Identify the blood parasite species.
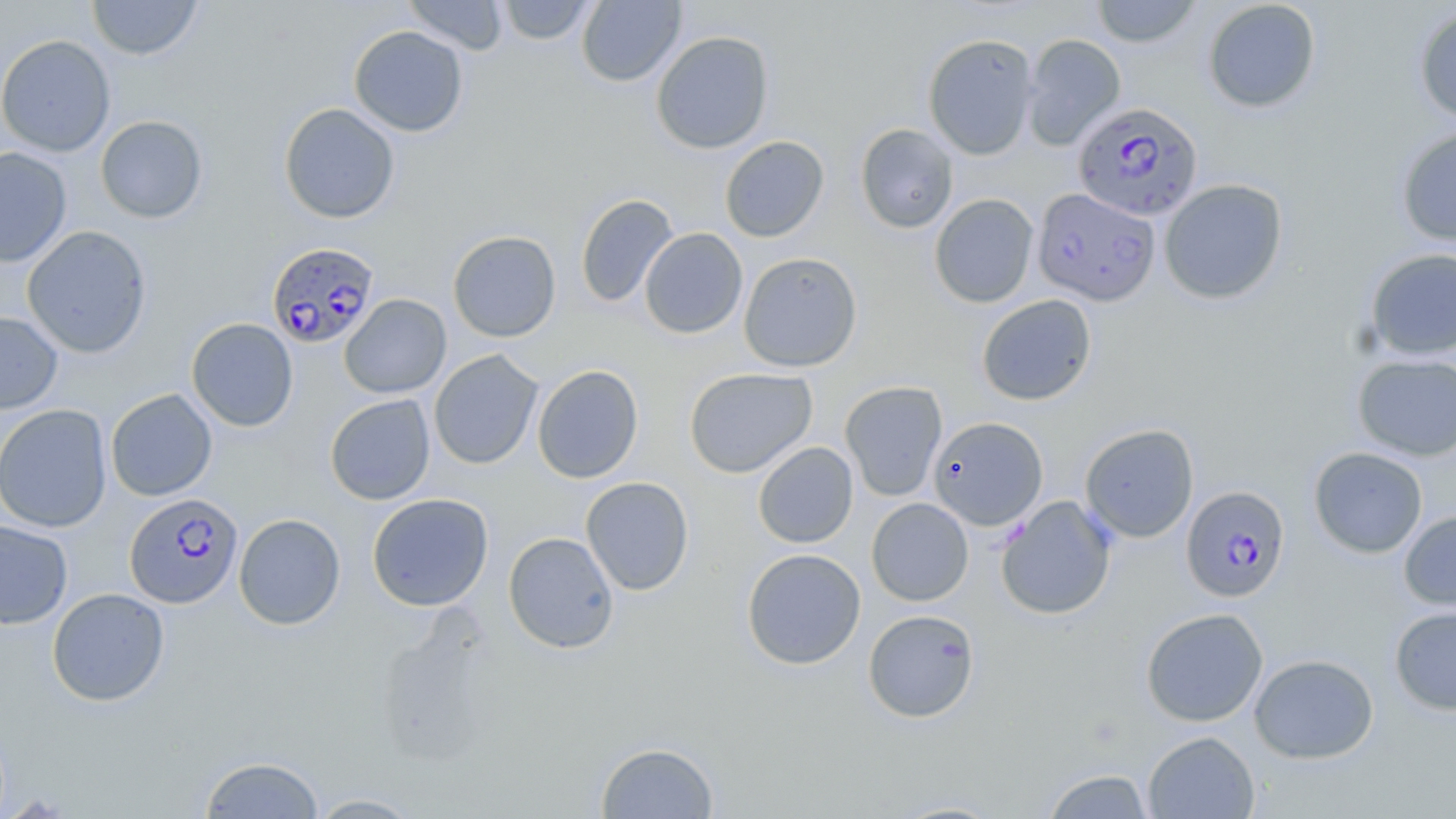
Plasmodium falciparum.

image size = 1456×819 pixels
magnification = 1000x
preparation = thin blood smear
Plasmodium falciparum-infected red blood cell locations = approximate bounding boxes as (x1, y1, x2, y2) in pixels: (1074, 101, 1203, 222), (1032, 187, 1161, 307), (266, 242, 381, 349), (1182, 485, 1290, 602), (125, 493, 243, 609)
field of view = one of a larger specimen
modality = optical microscopy
stain = May-Grünwald-Giemsa
uninfected red blood cell locations = approximate bounding boxes as (x1, y1, x2, y2) in pixels: (87, 0, 203, 60), (402, 0, 508, 55), (495, 0, 599, 45), (577, 0, 686, 87), (1090, 0, 1201, 48), (1202, 0, 1322, 113), (1413, 6, 1456, 125), (348, 25, 469, 137), (651, 30, 775, 154), (922, 33, 1039, 160), (0, 34, 116, 157), (1022, 34, 1126, 150), (279, 103, 400, 224), (95, 115, 208, 223), (855, 123, 959, 233), (1396, 125, 1456, 247), (719, 136, 829, 242), (0, 146, 72, 267), (1159, 179, 1288, 305), (575, 193, 679, 308), (929, 193, 1039, 308), (22, 225, 152, 358), (639, 228, 748, 339), (448, 230, 561, 342), (1364, 248, 1456, 360), (738, 252, 862, 372), (339, 293, 451, 398), (976, 294, 1097, 406), (0, 310, 63, 415), (186, 318, 299, 431), (429, 350, 543, 469), (1352, 353, 1456, 461), (532, 364, 643, 484), (684, 367, 817, 478), (840, 381, 948, 501), (106, 388, 217, 501), (325, 394, 436, 505), (0, 403, 113, 533), (929, 417, 1048, 530), (1080, 423, 1199, 542), (753, 441, 858, 548), (1308, 447, 1428, 558), (581, 476, 694, 595), (367, 493, 493, 611), (996, 495, 1116, 619), (866, 498, 974, 606), (1398, 509, 1456, 612), (233, 513, 346, 630), (0, 519, 73, 629), (503, 532, 619, 654), (742, 548, 866, 670), (47, 587, 169, 707), (1389, 605, 1456, 715), (863, 608, 980, 722), (1141, 608, 1268, 726), (1249, 653, 1379, 764), (1143, 731, 1259, 818), (595, 741, 720, 818), (199, 756, 325, 818), (1040, 769, 1156, 818), (307, 793, 424, 818), (884, 798, 1008, 818)